Identify the parasite.
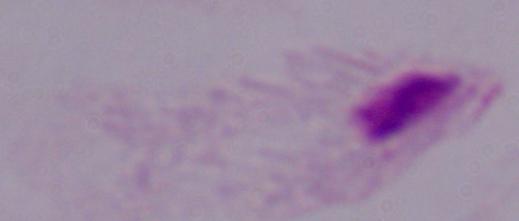

This is a trichomonad.

modality = photomicrograph
magnification = 1000x